Describe the morphology of the red blood cells.
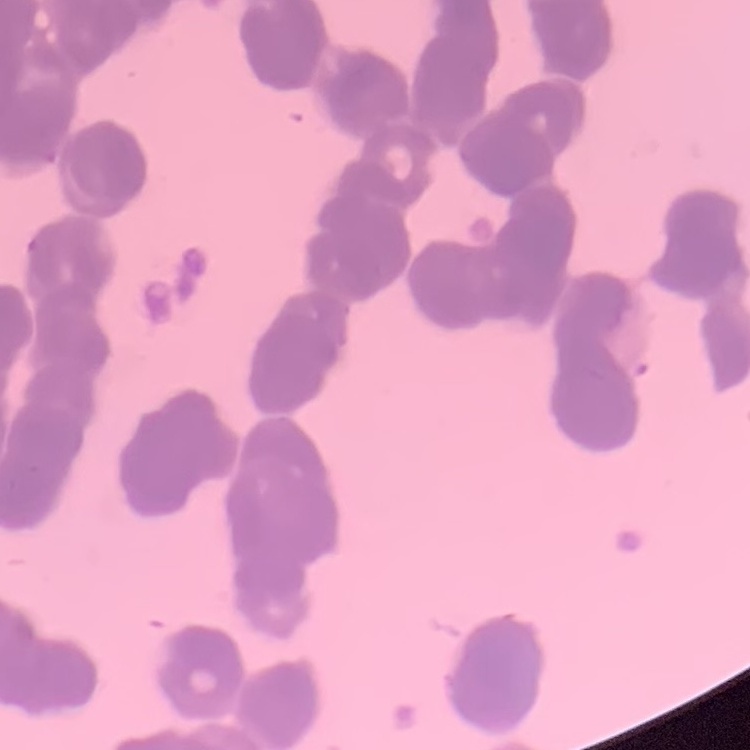
Rouleaux formation.

{
  "preparation": "thin blood film",
  "stain": "Field's or Giemsa",
  "image_type": "one tile cut from a larger photomicrograph"
}